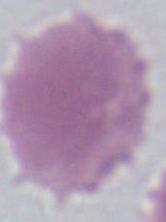

modality = photomicrograph
identification = erythrocyte
magnification = 1000x